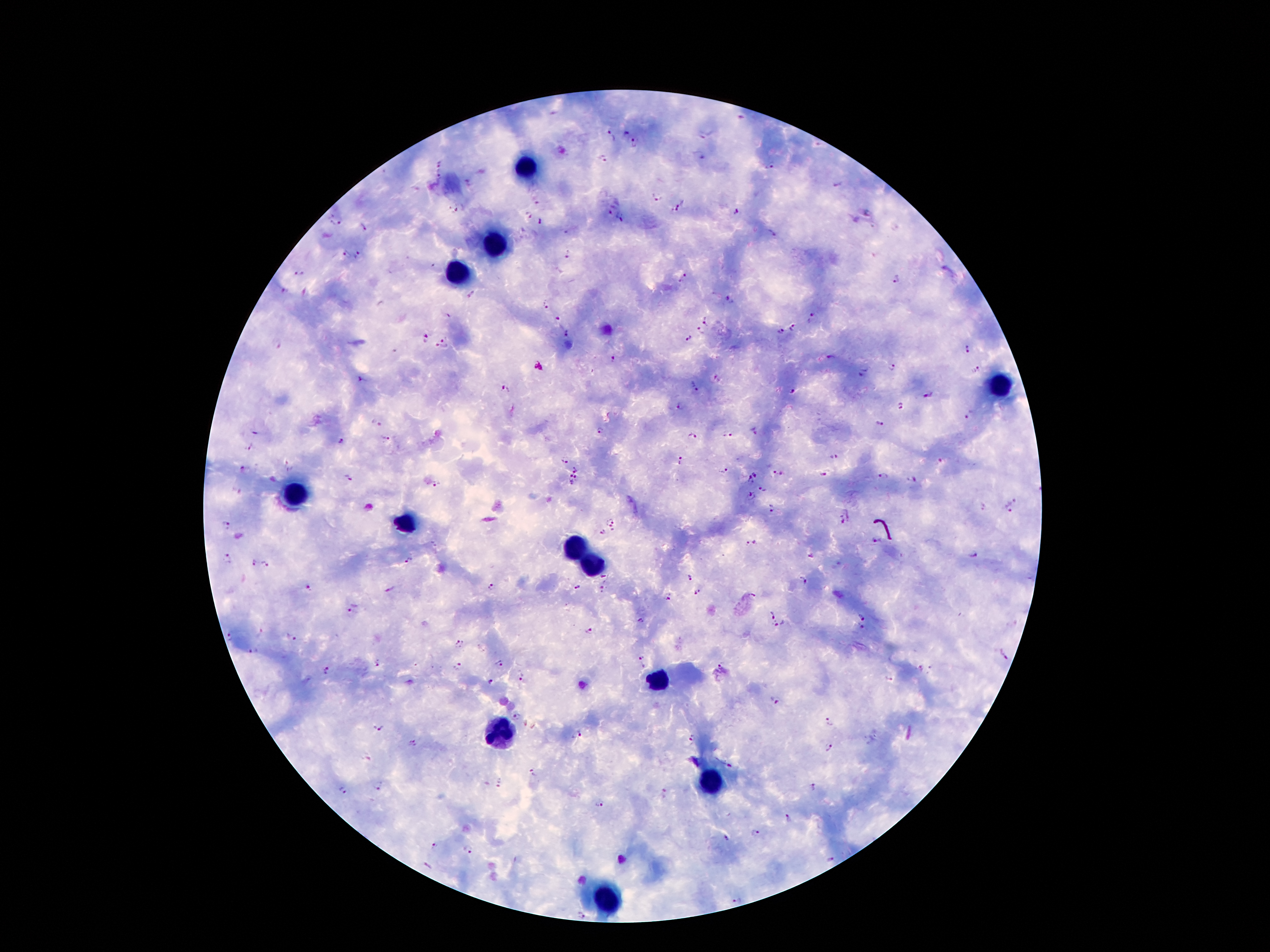

Approximate centers as {x, y} in pixels.
Summary:
  - Leukocyte locations: {525, 169}, {495, 249}, {459, 272}, {999, 385}, {295, 496}, {404, 524}, {572, 544}, {588, 562}, {652, 680}, {502, 737}, {706, 782}, {606, 896}
  - Plasmodium parasite locations: {552, 114}, {740, 116}, {626, 132}, {702, 134}, {610, 135}, {636, 143}, {699, 156}, {603, 159}, {441, 161}, {771, 166}, {437, 172}, {468, 184}, {839, 185}, {656, 195}, {537, 199}, {674, 209}, {460, 210}, {609, 210}, {734, 212}, {870, 214}, {527, 216}, {621, 217}, {336, 222}, {540, 223}, {363, 228}, {345, 255}, {359, 255}, {567, 255}, {297, 274}, {680, 278}, {895, 280}, {283, 291}, {472, 296}, {730, 299}, {547, 305}, {813, 315}, {557, 318}, {706, 321}, {793, 328}, {700, 329}, {781, 332}, {565, 333}, {446, 336}, {426, 337}, {689, 339}, {275, 344}, {442, 347}, {968, 350}, {394, 352}, {831, 357}, {613, 358}, {538, 367}, {894, 367}, {865, 369}, {977, 371}, {718, 379}, {362, 380}, {694, 386}, {505, 390}, {793, 390}, {931, 394}, {900, 406}, {680, 407}, {970, 415}, {880, 422}, {377, 424}, {256, 431}, {602, 431}, {755, 431}, {727, 435}, {692, 436}, {386, 440}, {340, 441}, {249, 450}, {835, 457}, {681, 460}, {565, 461}, {940, 461}, {289, 466}, {244, 468}, {576, 471}, {724, 471}, {756, 473}, {778, 474}, {823, 476}, {349, 478}, {882, 478}, {576, 479}, {751, 479}, {912, 479}, {567, 481}, {438, 486}, {762, 487}, {236, 491}, {752, 495}, {1014, 499}, {982, 505}, {1008, 507}, {773, 509}, {846, 517}, {611, 520}, {228, 524}, {603, 532}, {877, 540}, {752, 543}, {809, 555}, {973, 555}, {226, 560}, {408, 561}, {252, 564}, {266, 564}, {604, 575}, {690, 577}, {804, 579}, {491, 586}, {579, 587}, {309, 588}, {602, 589}, {389, 590}, {696, 592}, {667, 595}, {354, 610}, {771, 614}, {862, 617}, {641, 621}, {779, 625}, {860, 629}, {260, 631}, {588, 631}, {228, 638}, {291, 639}, {458, 644}, {253, 649}, {1004, 654}, {641, 658}, {376, 664}, {497, 664}, {722, 664}, {458, 667}, {932, 668}, {920, 669}, {326, 672}, {889, 678}, {521, 679}, {491, 683}, {776, 700}, {515, 716}, {829, 722}, {378, 726}, {576, 735}, {691, 740}, {412, 742}, {828, 748}, {366, 757}, {729, 765}, {532, 772}, {500, 783}, {379, 785}, {813, 789}, {343, 791}, {664, 795}, {599, 803}, {789, 819}, {755, 831}, {725, 836}, {432, 847}, {467, 850}, {427, 867}, {739, 900}, {581, 916}
  - Preparation: thick blood film
  - Stain: Giemsa
  - Image size: 1270×952 pixels
  - Patient malaria status: infected with Plasmodium falciparum
  - Capture: smartphone camera through the microscope eyepiece
  - Field of view: one from this slide
  - Magnification: 100x